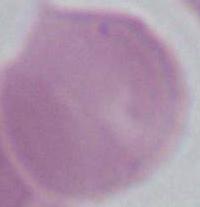 Captured at 1000x magnification. Micrograph. A red blood cell is shown.